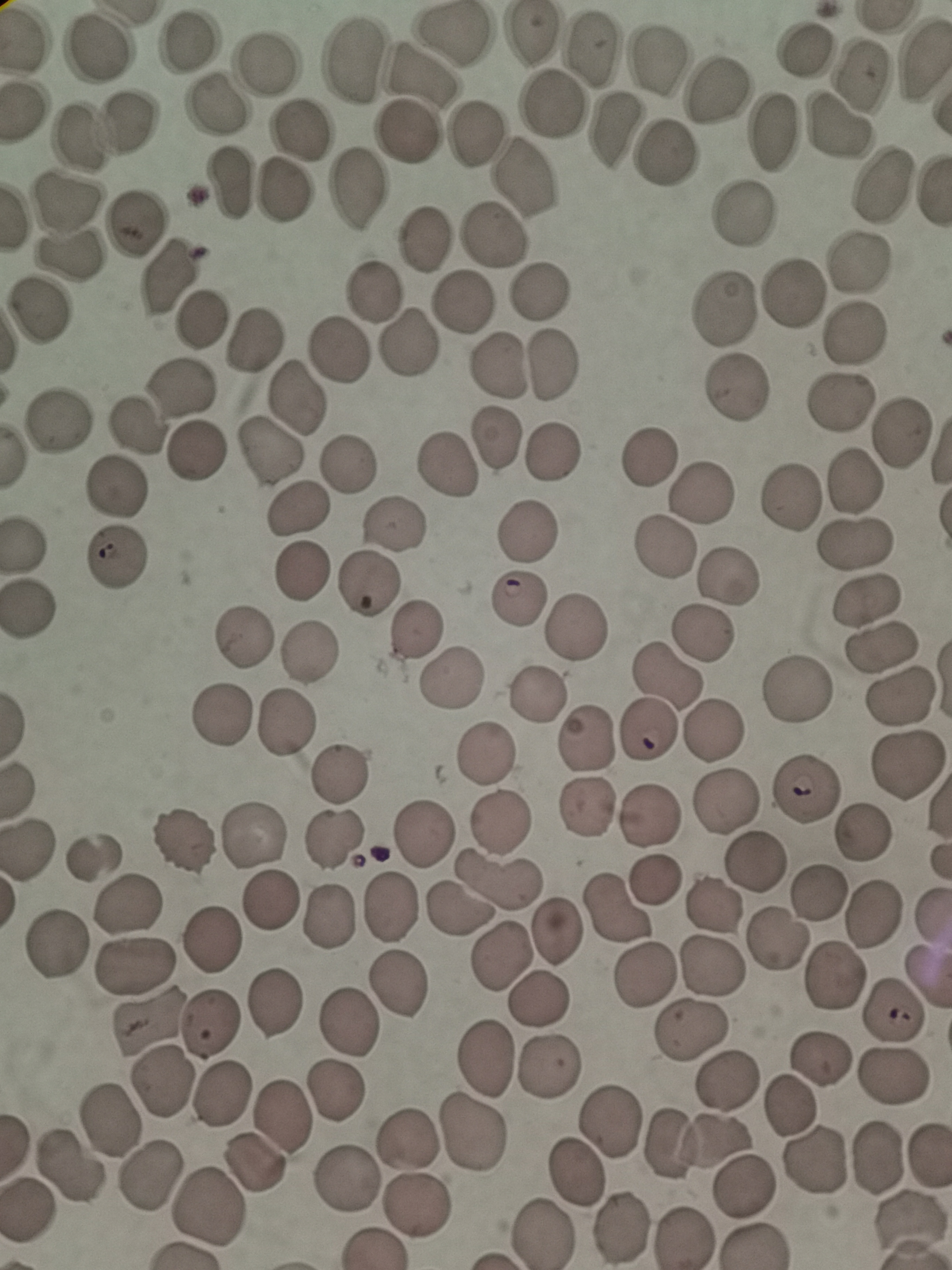
cell_locations: 'approximate centers as {x, y} in pixels: {453, 33}, {530, 35}, {183, 46}, {804, 46}, {99, 50}, {588, 51}, {659, 62}, {354, 63}, {267, 65}, {860, 73}, {422, 78}, {711, 92}, {211, 106}, {554, 108}, {130, 124}, {614, 126}, {838, 126}, {302, 129}, {772, 131}, {405, 134}, {471, 138}, {72, 140}, {667, 152}, {524, 181}, {881, 182}, {227, 187}, {360, 190}, {282, 194}, {65, 203}, {745, 210}, {135, 223}, {497, 238}, {423, 239}, {69, 254}, {859, 260}, {165, 282}, {791, 291}, {376, 295}, {538, 295}, {462, 301}, {723, 308}, {39, 310}, {200, 320}, {853, 332}, {252, 339}, {406, 344}, {337, 349}, {497, 362}, {554, 365}, {178, 386}, {736, 388}, {295, 396}, {839, 400}, {61, 420}, {131, 425}, {496, 435}, {900, 435}, {272, 446}, {188, 452}, {552, 453}, {647, 455}, {347, 463}, {447, 468}, {853, 481}, {114, 489}, {702, 490}, {791, 495}, {294, 507}, {393, 522}, {529, 529}, {854, 542}, {664, 544}, {112, 554}, {302, 569}, {731, 576}, {367, 581}, {517, 598}, {871, 600}, {32, 607}, {577, 625}, {414, 628}, {703, 634}, {240, 642}, {883, 645}, {307, 651}, {451, 677}, {665, 677}, {799, 687}, {535, 694}, {903, 699}, {222, 713}, {285, 724}, {644, 732}, {715, 732}, {585, 737}, {482, 753}, {908, 766}, {342, 772}, {805, 790}, {726, 800}, {588, 806}, {654, 815}, {500, 822}, {424, 831}, {256, 832}, {865, 832}, {337, 840}, {185, 841}, {29, 845}, {96, 854}, {756, 861}, {498, 881}, {660, 882}, {821, 893}, {266, 899}, {123, 905}, {715, 906}, {396, 908}, {618, 908}, {459, 910}, {873, 910}, {333, 913}, {560, 927}, {210, 937}, {781, 938}, {54, 943}, {505, 951}, {134, 959}, {714, 966}, {646, 975}, {834, 978}, {398, 984}, {539, 999}, {274, 1004}, {891, 1015}, {348, 1022}, {210, 1023}, {145, 1025}, {690, 1028}, {488, 1058}, {820, 1058}, {550, 1066}, {891, 1075}, {726, 1079}, {158, 1083}, {220, 1089}, {332, 1092}, {787, 1107}, {280, 1113}, {610, 1117}, {109, 1120}, {470, 1135}, {405, 1141}, {696, 1145}, {876, 1158}, {814, 1160}, {253, 1164}, {66, 1166}, {573, 1170}, {147, 1177}, {343, 1178}, {741, 1187}, {416, 1203}, {208, 1207}, {621, 1228}, {543, 1234}, {685, 1236}'
capture: smartphone through the microscope eyepiece
preparation: thin smear
image_size: 952×1270 pixels
field_of_view: single
stain: Giemsa